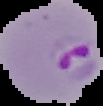 Image is 103×106 pixels. Result: Plasmodium parasites detected. From a thin blood film. Segmented cell region on a black background.